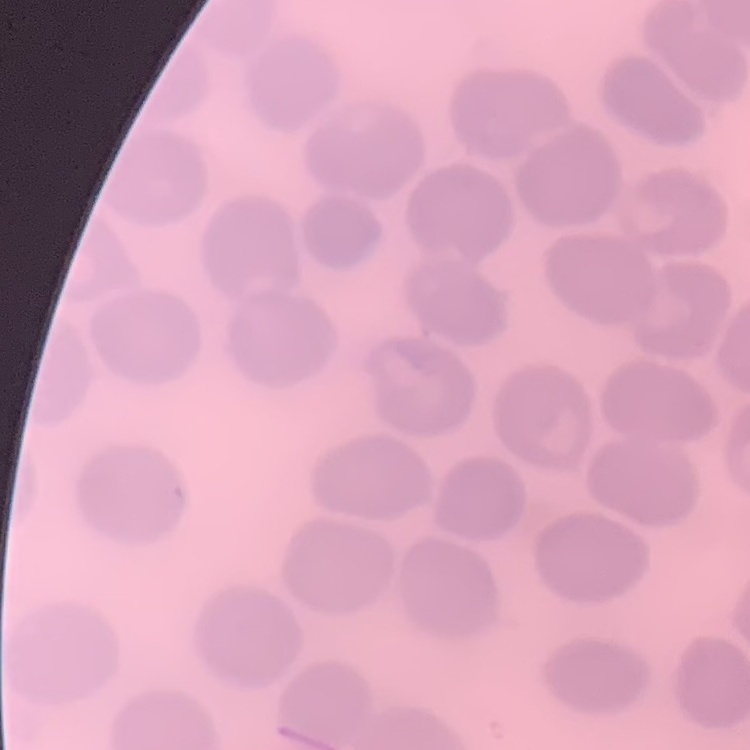

Summary:
  - Red blood cell morphology: no rouleaux formation
  - Preparation: thin blood smear
  - Image type: square crop of a larger photomicrograph
  - Stain: Field's or Giemsa